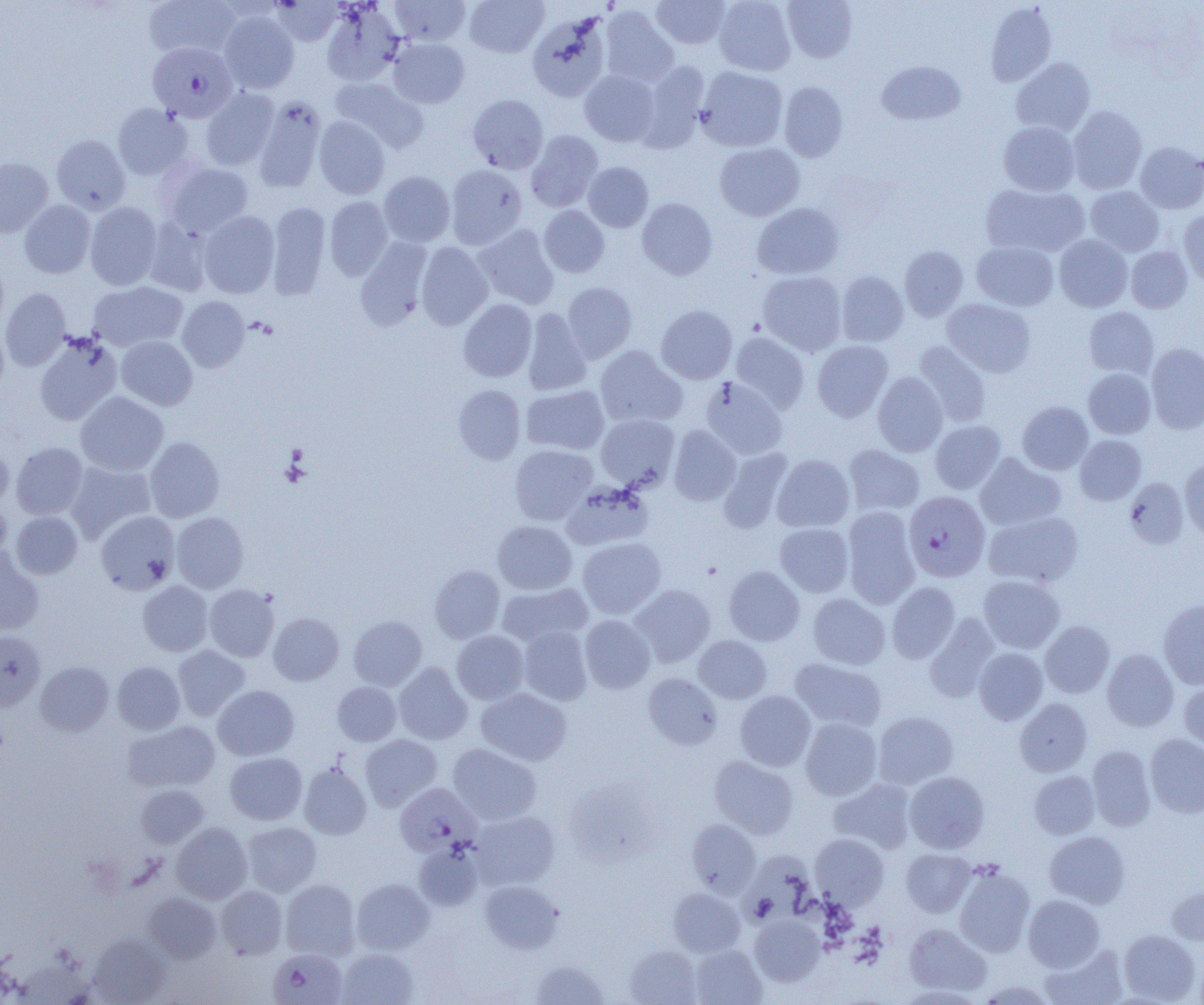

slide-level diagnosis = Plasmodium falciparum
image size = 1204×1005 pixels
Plasmodium falciparum-infected red blood cell locations = approximate bounding boxes as (x1, y1, x2, y2) in pixels: (148, 42, 237, 122), (904, 491, 990, 581), (394, 782, 481, 857), (267, 948, 347, 1005)
uninfected red blood cell locations = approximate bounding boxes as (x1, y1, x2, y2) in pixels: (144, 0, 238, 59), (273, 0, 342, 46), (390, 0, 470, 46), (464, 0, 548, 57), (651, 0, 731, 48), (714, 0, 796, 76), (782, 0, 858, 63), (985, 3, 1057, 87), (321, 4, 404, 86), (599, 6, 679, 87), (219, 11, 299, 93), (527, 11, 612, 102), (389, 38, 469, 108), (1011, 57, 1096, 137), (638, 60, 710, 150), (876, 61, 966, 125), (696, 66, 787, 152), (580, 70, 661, 146), (330, 76, 428, 152), (779, 81, 848, 162), (201, 88, 279, 170), (468, 94, 548, 173), (254, 96, 327, 193), (113, 104, 193, 180), (1067, 106, 1147, 194), (314, 117, 390, 199), (999, 121, 1080, 196), (526, 130, 603, 212), (51, 135, 130, 214), (715, 142, 805, 220), (1135, 142, 1204, 213), (0, 157, 53, 237), (162, 161, 254, 237), (582, 162, 653, 232), (445, 164, 526, 249), (379, 171, 455, 247), (980, 183, 1089, 257), (1086, 186, 1164, 256), (325, 196, 392, 280), (637, 198, 717, 280), (19, 200, 96, 278), (85, 202, 162, 290), (267, 202, 331, 300), (752, 203, 844, 279), (539, 206, 609, 278), (1179, 210, 1204, 287), (199, 211, 279, 298), (144, 220, 213, 297), (472, 224, 559, 310), (1054, 234, 1132, 312), (355, 239, 432, 331), (972, 241, 1059, 311), (416, 242, 493, 330), (899, 246, 968, 321), (1126, 246, 1193, 313), (0, 255, 9, 332), (758, 270, 847, 355), (836, 271, 909, 347), (88, 281, 188, 351), (562, 282, 638, 363), (1, 288, 71, 371), (177, 296, 250, 371), (942, 298, 1036, 377), (458, 299, 537, 382), (656, 305, 737, 383), (1084, 307, 1159, 378), (522, 308, 592, 396), (0, 321, 9, 403), (730, 332, 810, 413), (34, 334, 122, 426), (116, 336, 197, 410), (812, 340, 893, 422), (914, 341, 992, 427), (1146, 343, 1204, 433), (595, 345, 687, 428), (1083, 368, 1155, 439), (873, 372, 948, 457), (701, 377, 787, 459), (453, 385, 525, 464), (521, 385, 609, 455), (76, 392, 169, 476), (1017, 401, 1093, 474), (595, 414, 679, 490), (930, 420, 1006, 494), (669, 425, 741, 507), (1074, 435, 1147, 505), (144, 437, 225, 522), (0, 442, 13, 509), (11, 442, 88, 519), (843, 444, 925, 515), (510, 445, 597, 524), (717, 448, 792, 532), (975, 453, 1066, 531), (772, 454, 854, 532), (1180, 459, 1204, 539), (66, 460, 156, 542), (1124, 478, 1189, 549), (561, 483, 653, 550), (0, 495, 11, 564), (842, 507, 920, 608), (11, 511, 82, 579), (95, 511, 180, 595), (984, 511, 1083, 588), (171, 512, 248, 593), (493, 521, 577, 594), (775, 523, 854, 596), (578, 536, 666, 618), (0, 547, 44, 635), (430, 565, 505, 643), (724, 565, 805, 646), (979, 575, 1065, 653), (138, 581, 213, 656), (497, 582, 592, 647), (887, 582, 960, 663), (205, 584, 279, 662), (630, 584, 715, 667), (808, 594, 890, 669), (1158, 600, 1204, 689), (269, 612, 344, 686), (924, 614, 1000, 702), (349, 615, 426, 690), (579, 615, 655, 693), (1040, 621, 1115, 698), (518, 626, 592, 705), (0, 630, 45, 710), (452, 631, 529, 704), (694, 635, 772, 703), (173, 645, 250, 721), (974, 647, 1048, 725), (1102, 649, 1179, 731), (790, 657, 887, 732), (35, 661, 114, 736), (113, 662, 185, 734), (393, 662, 473, 745), (644, 673, 723, 750), (1179, 680, 1204, 754), (332, 682, 401, 745), (213, 685, 299, 760), (476, 688, 572, 766), (735, 691, 816, 770), (1014, 698, 1092, 776), (873, 711, 958, 789), (800, 718, 882, 800), (123, 720, 220, 792), (360, 734, 442, 811), (1145, 734, 1204, 817), (447, 744, 541, 824), (1087, 746, 1155, 830), (225, 752, 307, 824), (709, 756, 799, 839), (298, 760, 372, 839), (1029, 770, 1100, 839), (905, 771, 990, 853), (828, 779, 916, 854), (136, 784, 209, 848), (470, 810, 560, 890), (686, 820, 760, 897), (242, 821, 321, 896), (172, 822, 252, 904), (1044, 830, 1131, 908), (810, 833, 889, 909), (413, 841, 483, 911), (901, 848, 975, 917), (741, 850, 816, 925), (954, 866, 1035, 957), (352, 878, 435, 954), (281, 879, 360, 960), (479, 880, 563, 954), (1166, 885, 1204, 945), (216, 886, 288, 960), (668, 888, 744, 956), (144, 892, 222, 963), (1023, 895, 1105, 971), (750, 915, 825, 986), (903, 923, 992, 996), (1118, 929, 1200, 1003), (89, 934, 171, 1004), (1040, 944, 1128, 1005), (625, 945, 702, 1005), (690, 945, 766, 1004), (336, 948, 418, 1005), (530, 959, 610, 1004), (975, 979, 1054, 1004), (894, 985, 986, 1004)
magnification = 1000x
modality = optical microscopy
field of view = one of a larger specimen
preparation = thin blood film